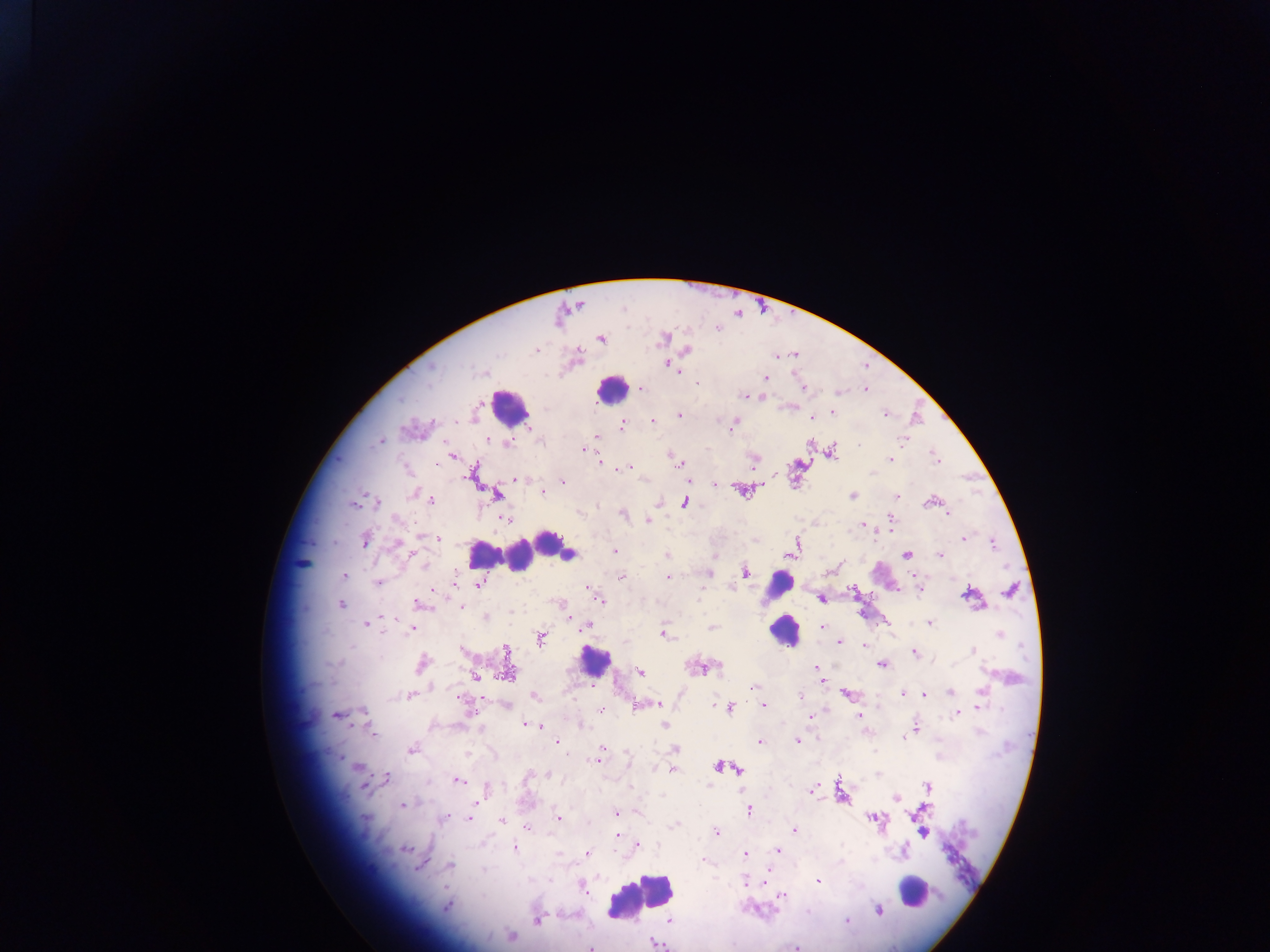
field_of_view: single
image_size: 1270×952 pixels
leukocyte_locations: 'approximate centers as (x, y) in pixels: (612, 389), (509, 407), (548, 545), (563, 552), (569, 553), (481, 554), (503, 554), (520, 556), (780, 584), (785, 630), (594, 660), (913, 891), (640, 896)'
capture: mobile-phone photograph through a microscope
country: Ghana
preparation: thick blood smear
plasmodium_parasite_locations: 'approximate centers as (x, y) in pixels: (717, 328), (663, 337), (600, 339), (686, 349), (536, 350), (792, 354), (776, 356), (668, 363), (765, 378), (641, 388), (804, 388), (865, 389), (838, 392), (747, 395), (760, 396), (832, 411), (679, 415), (884, 415), (812, 417), (653, 421), (733, 421), (621, 425), (597, 436), (488, 439), (904, 440), (380, 441), (507, 444), (583, 449), (830, 450), (452, 456), (891, 460), (598, 462), (937, 462), (680, 464), (630, 467), (473, 473), (516, 479), (688, 480), (562, 481), (742, 490), (542, 492), (495, 493), (852, 496), (897, 496), (430, 500), (932, 501), (375, 502), (659, 502), (684, 502), (353, 503), (622, 513), (948, 514), (506, 517), (890, 518), (647, 519), (862, 525), (438, 538), (964, 538), (365, 540), (792, 548), (614, 551), (410, 552), (907, 554), (667, 555), (940, 555), (302, 562), (745, 572), (708, 573), (344, 575), (620, 576), (667, 577), (915, 578), (377, 582), (479, 583), (1011, 589), (434, 590), (919, 590), (852, 591), (970, 595), (821, 598), (600, 599), (341, 603), (418, 603), (462, 607), (486, 616), (367, 622), (886, 623), (929, 623), (586, 626), (711, 627), (822, 627), (412, 628), (662, 633), (540, 638), (839, 641), (863, 646), (462, 650), (506, 650), (973, 650), (915, 653), (421, 663), (882, 664), (701, 667), (817, 669), (507, 671), (639, 672), (474, 675), (820, 676), (591, 685), (754, 686), (949, 692), (902, 693), (923, 693), (409, 695), (799, 695), (847, 695), (458, 696), (535, 696), (658, 704), (763, 704), (506, 705), (635, 705), (713, 705), (730, 707), (602, 710), (957, 712), (336, 714), (810, 716), (859, 717), (526, 724), (664, 724), (539, 726), (915, 727), (373, 732), (796, 740), (557, 741), (758, 741), (412, 748), (676, 749), (597, 758), (356, 766), (719, 766), (672, 768), (735, 768), (550, 773), (383, 778), (456, 779), (928, 787), (812, 789), (486, 790), (896, 796), (401, 804), (748, 809), (615, 813), (443, 817), (557, 818), (873, 818), (468, 819), (501, 820), (675, 825), (526, 827), (794, 830), (922, 831), (716, 833), (615, 835), (637, 846), (514, 848), (406, 849), (777, 850), (587, 852), (744, 854), (702, 861), (448, 866), (764, 878), (745, 881), (818, 881), (582, 887), (784, 895), (446, 906), (877, 909), (538, 919), (670, 919), (846, 921), (511, 936), (656, 942), (590, 946), (796, 946)'